Report the malaria status of this cell.
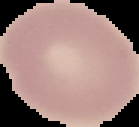
It is uninfected.

Summary:
  - Image size: 139×127 pixels
  - Image type: segmented cell region on a black background
  - Preparation: thin blood film